Assess this cell for malaria.
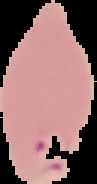
It is parasitized.

Summary:
  - Image size: 97×184 pixels
  - Image type: segmented cell region with the area outside set to black
  - Preparation: thin blood film